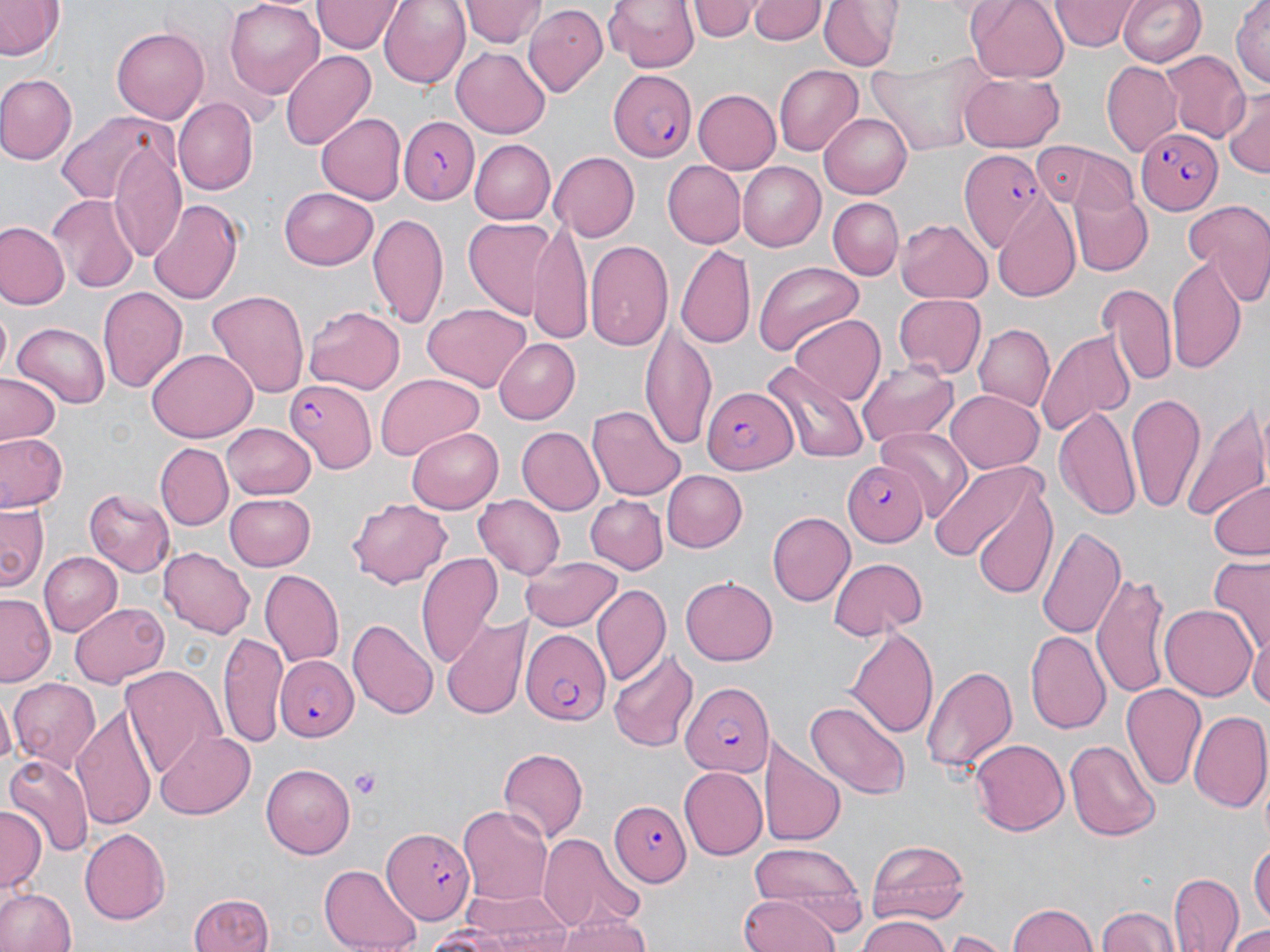

Summary:
  - Coordinate format: approximate bounding boxes as (x1, y1, x2, y2) in pixels
  - Uninfected red blood cell locations: (0, 0, 63, 63), (378, 0, 469, 88), (461, 0, 542, 50), (605, 0, 700, 73), (691, 0, 759, 41), (821, 0, 901, 71), (965, 0, 1070, 85), (1052, 0, 1135, 51), (1118, 0, 1207, 67), (1232, 0, 1269, 89), (224, 1, 323, 97), (313, 1, 400, 53), (747, 1, 827, 46), (524, 3, 608, 93), (112, 25, 208, 123), (452, 45, 550, 135), (279, 50, 375, 149), (1163, 51, 1252, 138), (869, 55, 994, 156), (1102, 61, 1181, 155), (773, 62, 863, 153), (959, 73, 1066, 150), (0, 74, 78, 166), (694, 88, 781, 172), (1223, 91, 1270, 176), (172, 100, 257, 194), (56, 111, 178, 207), (316, 111, 405, 203), (818, 112, 911, 198), (469, 139, 555, 224), (111, 142, 188, 261), (1062, 148, 1145, 252), (550, 151, 640, 242), (662, 159, 746, 247), (738, 162, 826, 250), (1070, 186, 1154, 274), (279, 187, 379, 269), (47, 192, 139, 293), (826, 196, 903, 278), (1181, 197, 1270, 305), (995, 198, 1084, 304), (148, 199, 242, 306), (368, 210, 448, 326), (463, 218, 556, 321), (897, 219, 993, 303), (1, 222, 68, 309), (529, 222, 592, 339), (586, 239, 673, 355), (677, 243, 754, 348), (1167, 254, 1247, 375), (754, 260, 866, 358), (1097, 281, 1177, 387), (97, 286, 187, 393), (206, 289, 310, 398), (892, 294, 987, 379), (424, 303, 532, 393), (305, 304, 406, 393), (1, 310, 15, 382), (789, 315, 884, 406), (13, 322, 112, 405), (642, 322, 716, 447), (974, 324, 1054, 411), (1036, 330, 1136, 431), (493, 338, 579, 423), (147, 347, 256, 441), (762, 363, 869, 464), (857, 364, 961, 447), (374, 374, 487, 459), (1, 375, 63, 445), (948, 389, 1043, 473), (1126, 392, 1209, 515), (1184, 401, 1270, 524), (589, 406, 685, 500), (1055, 406, 1141, 520), (222, 424, 317, 500), (406, 427, 501, 514), (518, 427, 603, 516), (876, 427, 972, 518), (0, 432, 67, 512), (158, 444, 231, 527), (927, 457, 1050, 566), (661, 471, 748, 551), (968, 476, 1057, 600), (1209, 479, 1270, 560), (87, 490, 173, 575), (223, 492, 315, 571), (473, 495, 566, 581), (584, 496, 668, 575), (348, 497, 454, 589), (0, 505, 47, 589), (768, 511, 855, 606), (1035, 524, 1126, 638), (159, 548, 256, 637), (37, 551, 121, 637), (416, 551, 503, 668), (523, 554, 624, 632), (1206, 557, 1270, 655), (829, 558, 927, 639), (259, 569, 343, 667), (1094, 571, 1170, 697), (679, 577, 779, 666), (590, 582, 670, 684), (1, 592, 57, 685), (70, 601, 168, 686), (1161, 604, 1257, 701), (442, 610, 528, 721), (347, 620, 438, 720), (846, 626, 938, 739), (1027, 629, 1112, 734), (218, 633, 287, 745), (1248, 636, 1270, 714), (608, 648, 700, 753), (921, 663, 1019, 776), (121, 665, 225, 777), (9, 679, 102, 769), (1122, 683, 1208, 794), (1, 694, 16, 771), (804, 698, 910, 800), (75, 704, 157, 831), (1188, 710, 1270, 812), (155, 730, 256, 819), (763, 736, 843, 850), (1065, 738, 1160, 840), (969, 739, 1069, 836), (498, 746, 589, 841), (5, 754, 92, 858), (261, 761, 356, 855), (678, 767, 766, 859), (458, 803, 553, 909), (0, 806, 44, 893), (80, 828, 171, 923), (536, 834, 645, 932), (866, 838, 972, 925), (1252, 841, 1269, 932), (745, 842, 870, 926), (322, 863, 421, 952), (1169, 871, 1244, 952), (0, 888, 75, 952), (464, 888, 573, 948), (188, 893, 274, 952), (739, 894, 837, 952), (1006, 902, 1100, 952), (1098, 906, 1179, 952), (857, 914, 950, 952), (553, 917, 653, 952), (418, 924, 517, 951), (1225, 925, 1270, 952), (944, 931, 1011, 952)
  - Plasmodium falciparum-infected red blood cell locations: (604, 72, 697, 161), (397, 114, 479, 205), (1136, 128, 1221, 213), (958, 150, 1050, 250), (284, 378, 375, 471), (703, 385, 799, 475), (841, 462, 928, 547), (521, 629, 609, 726), (274, 653, 357, 742), (679, 680, 770, 776), (611, 799, 689, 888), (381, 826, 474, 925)
  - Platelet locations: (349, 767, 384, 798)
  - Slide-level diagnosis: Plasmodium falciparum
  - Stain: May-Grünwald-Giemsa
  - Image size: 1270×952 pixels
  - Modality: light microscopy
  - Preparation: thin blood smear
  - Magnification: 1000x
  - Field of view: one of a larger specimen